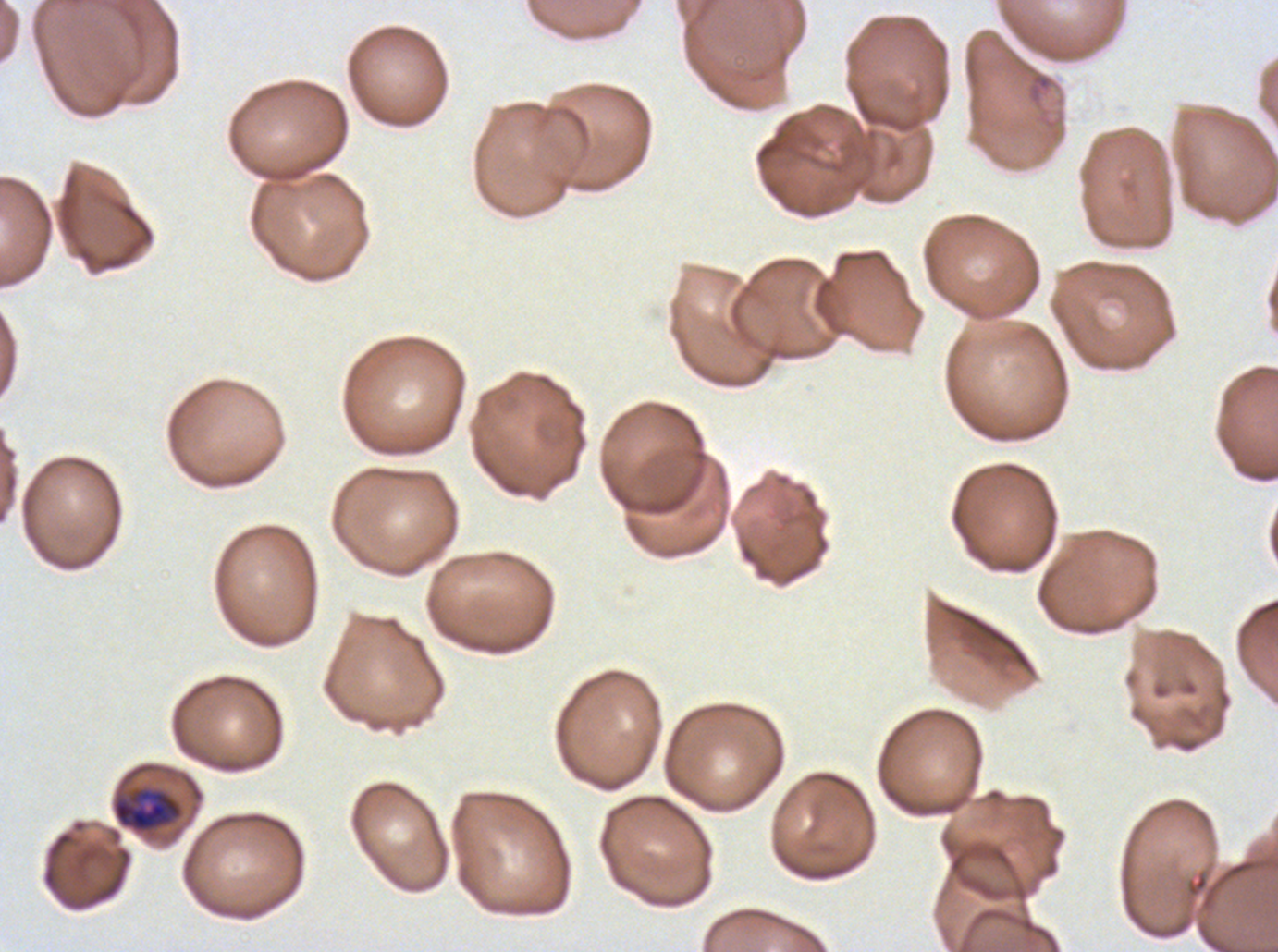

Approximate bounding boxes as [x1, y1, x2, y2] in pixels.
Summary:
  - Mid trophozoite locations: [112, 787, 183, 833]
  - Stain: Giemsa
  - Image size: 1278×952 pixels
  - Field of view: one sub-image of a larger composite
  - Preparation: thin blood smear
  - Specimen: ex-vivo Plasmodium falciparum culture from a patient in The Gambia, grown for 24 to 48 hours